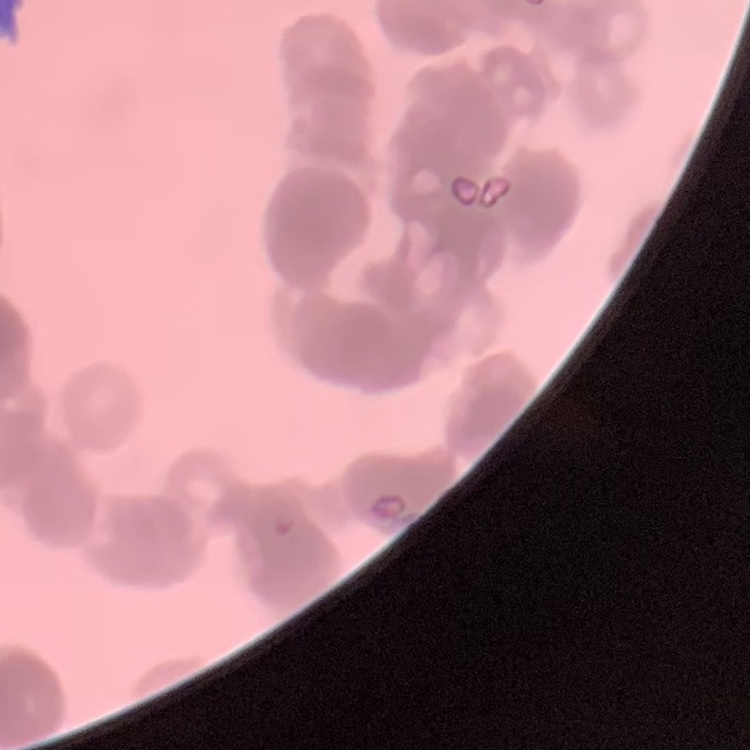

The erythrocytes exhibit rouleaux formation. One tile cut from a larger photomicrograph. Field's or Giemsa stain. Thin peripheral smear.